State the blood parasite species.
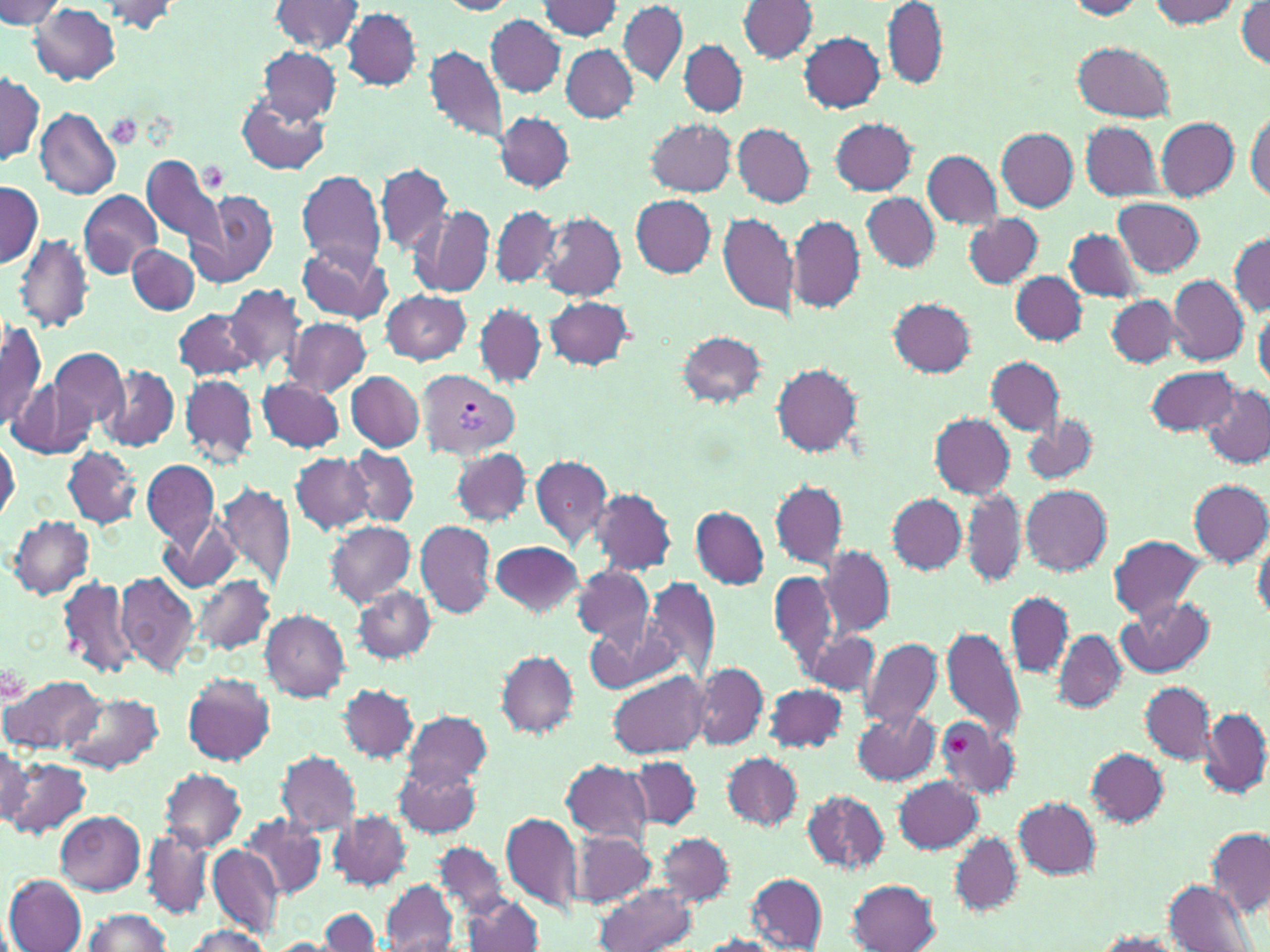

Plasmodium vivax.

Approximate bounding boxes as (x1,y1)-(x2,y2) corner pairs in pixels. Uninfected red blood cell locations: (0,1)-(68,28), (89,1)-(187,33), (270,1)-(364,53), (438,1)-(518,15), (538,1)-(623,40), (618,1)-(687,86), (1063,1)-(1150,19), (1142,1)-(1244,28), (740,2)-(818,63), (1236,2)-(1269,72), (29,3)-(121,85), (883,3)-(946,90), (343,8)-(421,90), (486,15)-(565,96), (799,32)-(885,113), (679,40)-(747,118), (1073,41)-(1175,122), (425,46)-(507,142), (562,46)-(638,123), (259,47)-(342,124), (0,70)-(44,168), (238,92)-(329,176), (34,108)-(121,199), (1246,109)-(1269,202), (496,112)-(573,192), (645,118)-(736,196), (830,118)-(917,195), (1155,118)-(1239,199), (1081,121)-(1161,200), (733,122)-(815,207), (998,128)-(1077,211), (922,149)-(1002,229), (141,153)-(224,252), (376,161)-(452,254), (296,170)-(386,271), (0,183)-(41,268), (187,188)-(279,289), (78,190)-(162,279), (862,191)-(939,272), (629,194)-(716,277), (1113,197)-(1204,276), (410,206)-(495,298), (491,206)-(560,289), (718,211)-(799,318), (540,212)-(625,301), (964,214)-(1044,288), (788,215)-(863,312), (1065,228)-(1144,303), (16,234)-(93,333), (1230,234)-(1269,317), (295,239)-(391,323), (128,243)-(200,316), (1011,272)-(1087,345), (1168,275)-(1249,364), (222,282)-(310,379), (380,290)-(471,363), (1106,295)-(1185,369), (544,296)-(633,371), (889,298)-(976,376), (474,303)-(547,388), (1254,308)-(1269,389), (172,309)-(258,381), (0,318)-(47,432), (285,318)-(371,396), (675,329)-(767,408), (48,346)-(129,434), (986,357)-(1065,435), (771,361)-(862,456), (99,366)-(179,451), (1146,366)-(1240,436), (346,371)-(424,451), (180,374)-(258,464), (256,377)-(345,452), (8,380)-(93,459), (1200,384)-(1270,469), (1022,411)-(1099,485), (931,413)-(1014,497), (0,435)-(19,522), (62,444)-(144,527), (345,447)-(418,526), (450,448)-(531,525), (292,451)-(373,533), (530,454)-(612,550), (142,459)-(219,547), (770,480)-(847,570), (1189,481)-(1269,567), (216,482)-(295,592), (1021,485)-(1112,576), (962,486)-(1026,587), (591,488)-(676,576), (886,493)-(966,575), (691,507)-(769,588), (160,513)-(241,593), (9,515)-(94,598), (415,520)-(496,617), (326,521)-(416,607), (1108,535)-(1207,622), (1252,538)-(1270,623), (490,541)-(584,617), (819,545)-(895,639), (573,565)-(655,646), (769,568)-(838,672), (113,571)-(198,677), (191,573)-(276,655), (57,574)-(138,679), (643,578)-(719,679), (354,587)-(435,662), (1005,593)-(1072,678), (1119,598)-(1215,679), (261,610)-(350,701), (586,615)-(674,694), (941,624)-(1026,743), (806,631)-(881,695), (1053,631)-(1126,712), (861,636)-(943,730), (496,652)-(577,737), (694,663)-(767,748), (608,670)-(710,760), (183,672)-(276,766), (3,675)-(102,755), (1140,681)-(1214,764), (764,683)-(848,753), (339,684)-(417,763), (63,691)-(163,774), (1200,708)-(1269,798), (402,709)-(492,791), (853,709)-(942,786), (935,718)-(1018,800), (0,741)-(32,827), (1087,749)-(1168,825), (277,751)-(362,835), (723,752)-(803,830), (2,756)-(91,838), (628,756)-(701,829), (561,759)-(653,841), (395,761)-(483,839), (160,768)-(247,852), (894,776)-(984,853), (800,789)-(890,875), (1013,798)-(1100,878), (56,810)-(146,895), (330,811)-(411,889), (500,811)-(584,916), (243,814)-(325,899), (143,826)-(213,919), (573,828)-(656,909), (1207,828)-(1269,916), (948,831)-(1022,915), (656,833)-(734,907), (435,842)-(507,918), (207,844)-(282,941), (747,873)-(828,950), (4,874)-(86,952), (846,879)-(941,952), (380,880)-(459,952), (1163,880)-(1257,952), (591,883)-(699,952), (463,893)-(543,952), (318,908)-(382,952), (80,909)-(174,951), (180,926)-(274,951), (1091,932)-(1185,951), (696,934)-(787,952), (271,937)-(333,952). Plasmodium vivax-infected red blood cell locations: (419,371)-(520,458). Platelet locations: (109,115)-(142,149), (199,162)-(227,191), (945,731)-(976,757). Captured at 1000x magnification. May-Grünwald-Giemsa-stained preparation. Light microscopy. Single field of view. Image is 1270×952 pixels. Thin blood film.